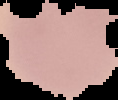
image type = segmented cell region on a black background
result = no malaria parasites detected
image size = 118×100 pixels
preparation = thin blood film